Report the malaria status of this cell.
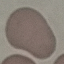

Uninfected.

Thin blood smear. Automatically extracted cell patch, resized to 64 × 64 pixels. Giemsa stain. Photographed with a smartphone camera at the microscope eyepiece.